Assess the morphology of the erythrocytes.
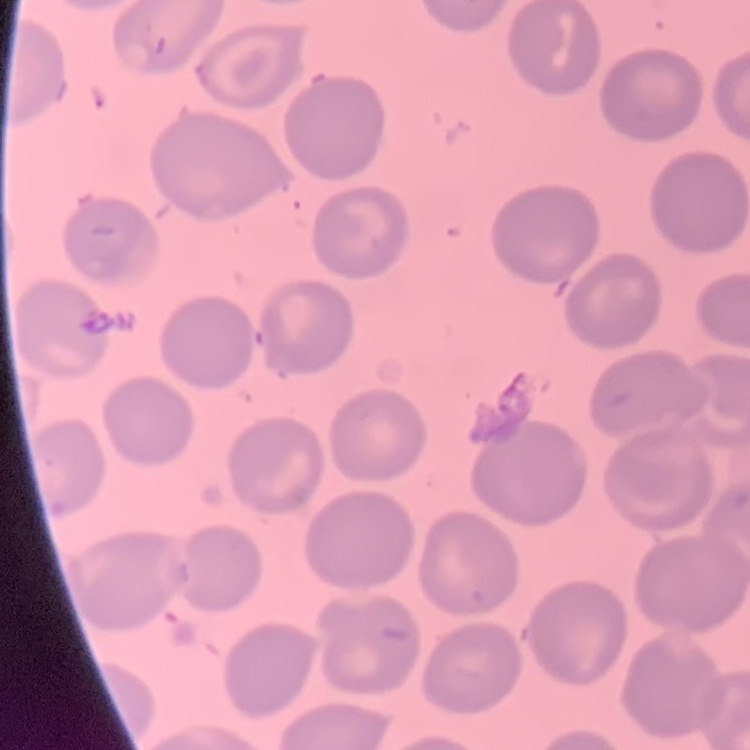

They show no rouleaux formation.

Summary:
  - Preparation: thin blood film
  - Stain: Field's or Giemsa
  - Image type: one tile cut from a larger photomicrograph